Identify the cell.
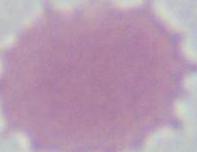
This is an erythrocyte.

Summary:
  - Magnification: 1000x
  - Modality: photomicrograph